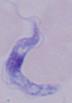

magnification = 1000x
identification = trypanosome
modality = micrograph